Identify the blood parasite species.
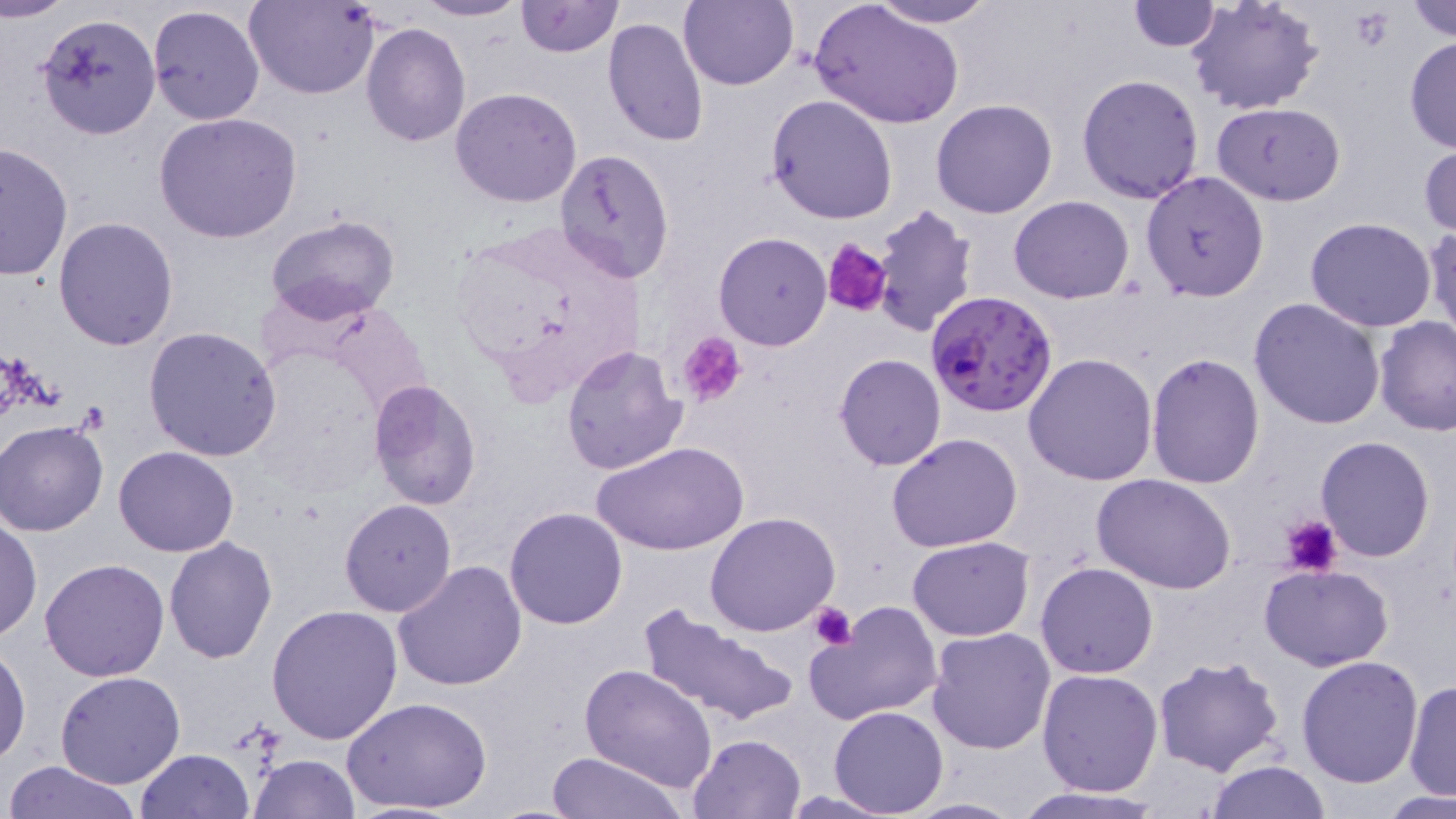

Plasmodium falciparum.

Approximate bounding boxes as (x1, y1, x2, y2) in pixels. Uninfected red blood cell locations: (3, 0, 71, 22), (412, 0, 529, 22), (679, 0, 798, 91), (867, 0, 999, 27), (1186, 0, 1324, 116), (1406, 0, 1456, 43), (246, 1, 379, 99), (513, 1, 623, 57), (1128, 1, 1221, 51), (808, 2, 964, 129), (145, 4, 264, 127), (37, 12, 160, 139), (601, 15, 709, 147), (361, 22, 470, 147), (1405, 35, 1456, 156), (1076, 75, 1205, 205), (450, 87, 583, 207), (766, 94, 898, 225), (931, 99, 1059, 220), (1211, 101, 1346, 205), (154, 113, 303, 244), (1419, 141, 1456, 238), (0, 143, 73, 283), (552, 147, 675, 283), (1140, 171, 1270, 303), (1009, 196, 1135, 304), (870, 204, 979, 335), (264, 214, 402, 323), (53, 217, 179, 353), (1304, 217, 1437, 332), (1424, 220, 1456, 349), (714, 232, 831, 350), (1248, 297, 1387, 431), (1375, 317, 1456, 438), (143, 327, 282, 463), (561, 344, 687, 475), (1147, 351, 1265, 488), (833, 352, 946, 471), (1022, 352, 1158, 485), (367, 381, 481, 509), (0, 421, 107, 537), (886, 434, 1024, 553), (1316, 434, 1437, 560), (593, 440, 749, 556), (113, 446, 240, 557), (1092, 474, 1238, 594), (338, 498, 458, 617), (504, 506, 630, 629), (704, 513, 842, 636), (0, 518, 41, 642), (165, 535, 277, 662), (908, 536, 1033, 639), (39, 559, 169, 682), (392, 560, 527, 692), (1035, 562, 1159, 679), (1259, 562, 1395, 672), (809, 602, 944, 727), (266, 604, 404, 745), (637, 604, 798, 730), (926, 627, 1055, 754), (0, 643, 31, 768), (1153, 653, 1285, 775), (1296, 657, 1424, 789), (582, 664, 718, 791), (1036, 668, 1163, 794), (55, 673, 184, 790), (1404, 680, 1454, 801), (342, 695, 493, 815), (828, 705, 948, 816), (687, 733, 805, 818), (134, 748, 255, 818), (547, 750, 686, 819), (247, 753, 361, 818), (1203, 759, 1334, 817), (4, 761, 144, 819), (1007, 788, 1169, 818), (772, 790, 906, 818), (1383, 792, 1453, 817), (900, 796, 1026, 817). Plasmodium falciparum-infected red blood cell locations: (925, 291, 1058, 418). Platelet locations: (823, 237, 893, 318), (680, 332, 746, 408), (1282, 514, 1342, 577), (809, 601, 857, 650). Optical microscopy. Single field of view. Image is 1456×819 pixels. Thin blood smear. 1000x magnification. May-Grünwald-Giemsa-stained preparation.